Locate and identify every blood parasite.
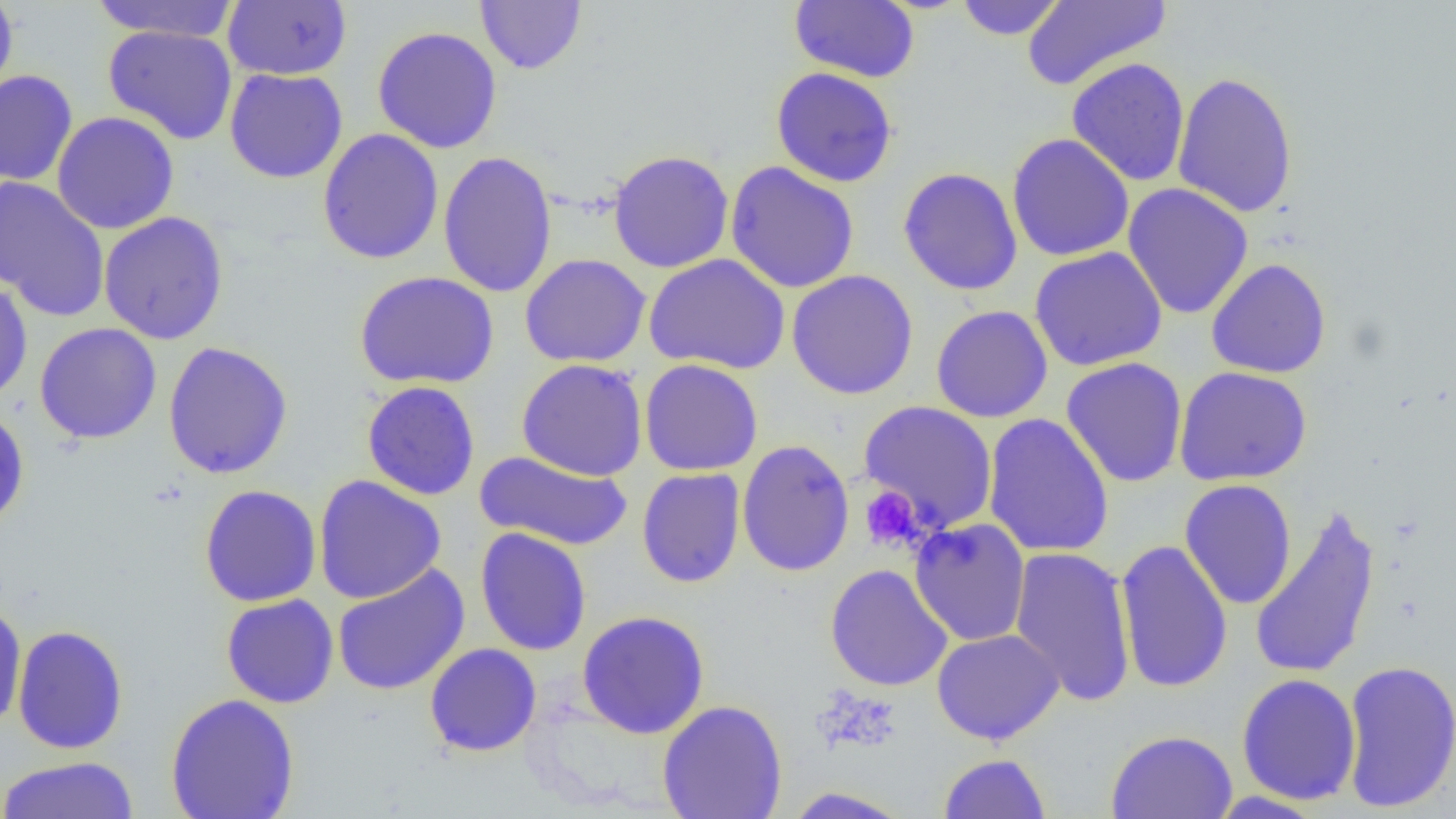
No blood parasites seen.

Approximate bounding boxes as [x1, y1, x2, y2] in pixels. Platelet locations: [859, 487, 925, 551]. Uninfected red blood cell locations: [88, 0, 241, 41], [222, 0, 352, 81], [476, 0, 587, 75], [789, 0, 920, 83], [954, 0, 1069, 40], [0, 1, 19, 102], [1022, 1, 1172, 91], [103, 25, 238, 145], [372, 26, 503, 154], [1066, 57, 1190, 187], [770, 67, 899, 187], [224, 68, 348, 184], [0, 70, 78, 187], [1172, 71, 1299, 218], [52, 111, 179, 234], [317, 128, 444, 265], [1006, 133, 1135, 261], [607, 150, 735, 272], [438, 151, 557, 298], [725, 160, 860, 294], [898, 167, 1023, 296], [0, 176, 110, 323], [1122, 182, 1254, 320], [98, 211, 229, 345], [1028, 247, 1167, 371], [519, 253, 651, 368], [644, 254, 791, 375], [1206, 258, 1332, 378], [354, 270, 499, 390], [786, 270, 919, 400], [0, 276, 33, 405], [931, 305, 1053, 423], [34, 322, 163, 444], [163, 341, 293, 480], [1060, 357, 1188, 488], [515, 359, 648, 481], [639, 359, 763, 476], [1174, 366, 1312, 487], [361, 380, 481, 501], [858, 400, 999, 534], [0, 405, 30, 532], [983, 412, 1114, 559], [736, 439, 855, 577], [474, 450, 633, 551], [636, 468, 746, 588], [313, 474, 447, 604], [1179, 479, 1297, 610], [199, 484, 322, 607], [1248, 503, 1383, 683], [909, 517, 1031, 646], [475, 527, 592, 656], [1114, 538, 1233, 694], [1009, 546, 1137, 707], [332, 564, 471, 696], [825, 564, 953, 692], [221, 594, 339, 708], [0, 600, 27, 732], [577, 610, 710, 739], [12, 624, 128, 754], [932, 628, 1065, 744], [424, 643, 542, 757], [1340, 659, 1456, 813], [1236, 673, 1362, 805], [165, 693, 300, 819], [658, 700, 787, 819], [1107, 730, 1238, 819], [938, 753, 1051, 818], [0, 756, 141, 819], [781, 787, 915, 818], [1206, 791, 1329, 818]. Slide-level diagnosis: negative for blood parasites. One field of a larger specimen. Image is 1456×819 pixels. Light microscopy. Thin blood smear. 1000x magnification.